Identify the parasite.
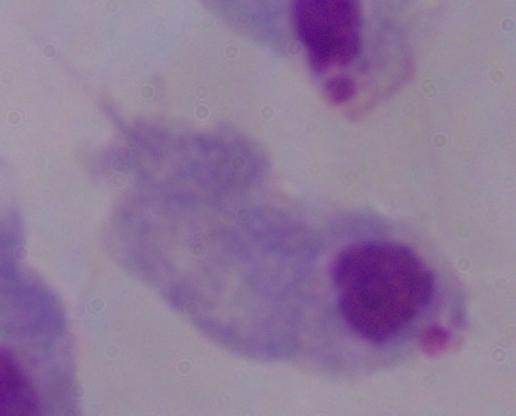
A trichomonad.

magnification = 1000x
modality = photomicrograph